State which parasite is depicted.
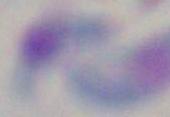

This is Toxoplasma gondii.

magnification = 1000x
modality = photomicrograph